Assess this cell for malaria.
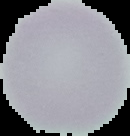

It is uninfected.

Segmented cell region on a black background. Image is 130×136 pixels. From a thin blood smear.